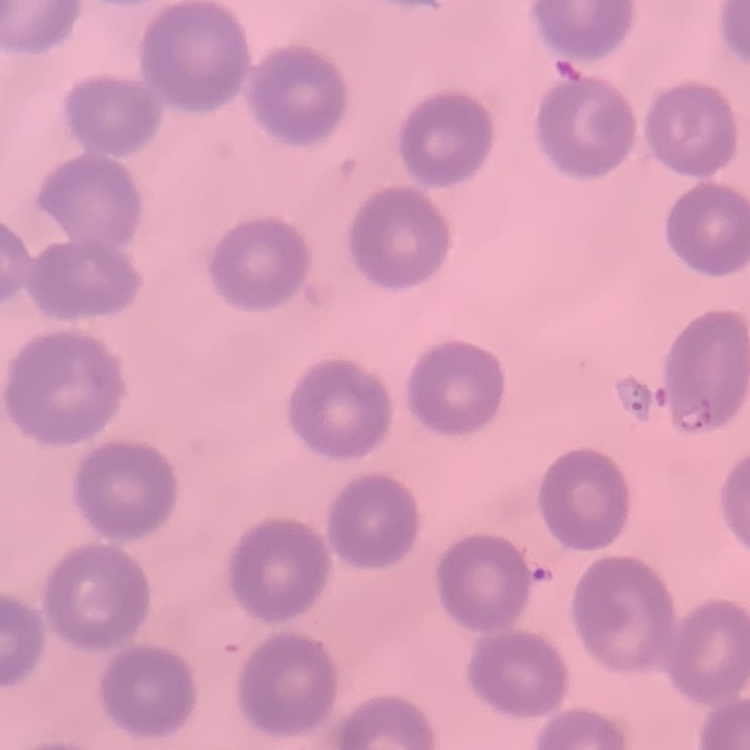 The red blood cells show no rouleaux formation. One tile cut from a larger photomicrograph. Stained with either Field's or Giemsa. Thin peripheral smear.